Comment on the morphology of the erythrocytes.
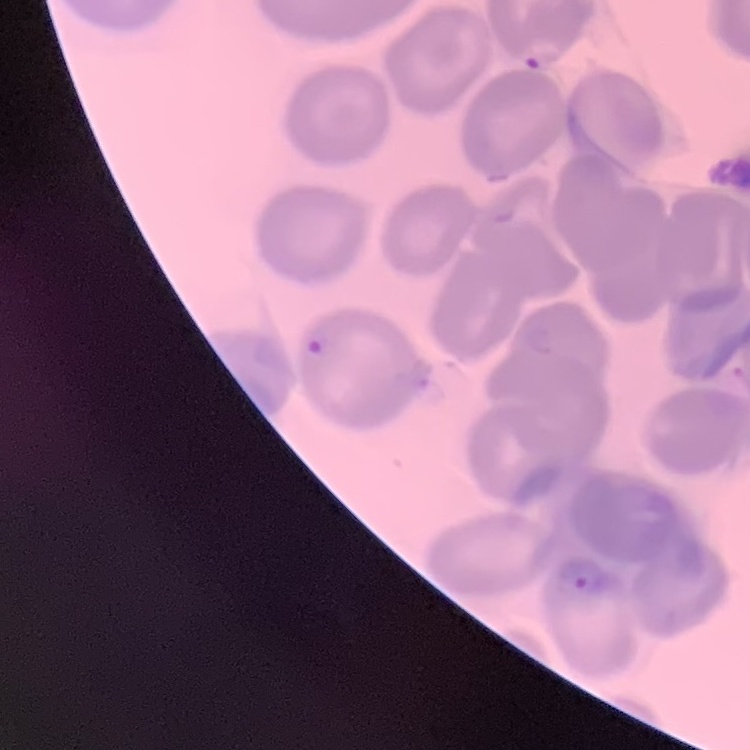

They show no rouleaux formation.

stain = Field's or Giemsa
preparation = thin blood smear
image type = square crop of a larger photomicrograph